Report the malaria status of this cell.
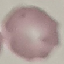
Uninfected.

preparation: thin blood film
capture: smartphone through the microscope eyepiece
image_type: cell patch, automatically extracted from a larger field of view and resized to 64 × 64 pixels
stain: Giemsa